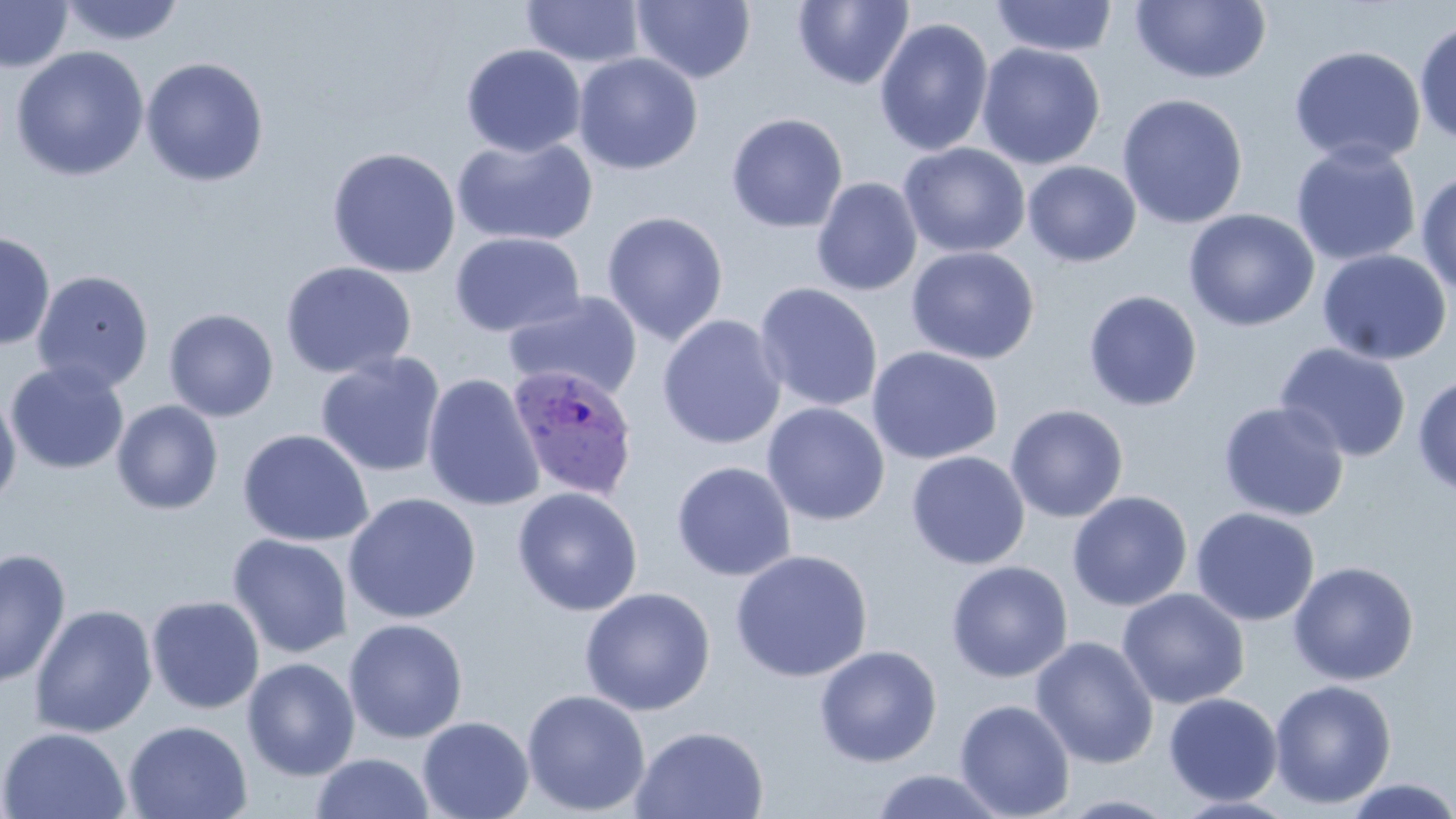 Approximate bounding boxes as [x1, y1, x2, y2] in pixels. Plasmodium ovale-infected red blood cell locations: [506, 364, 639, 501]. Uninfected red blood cell locations: [793, 0, 915, 91], [989, 0, 1119, 58], [0, 1, 73, 72], [58, 1, 187, 47], [519, 1, 646, 68], [631, 1, 757, 84], [1130, 2, 1271, 84], [874, 17, 994, 157], [1413, 19, 1456, 147], [976, 42, 1106, 170], [460, 43, 586, 158], [1288, 44, 1426, 169], [11, 46, 149, 181], [573, 52, 703, 175], [140, 57, 269, 186], [1116, 93, 1249, 229], [726, 113, 848, 233], [452, 135, 598, 248], [1290, 141, 1422, 267], [898, 142, 1031, 259], [326, 147, 461, 279], [1023, 161, 1141, 267], [1415, 170, 1456, 297], [811, 177, 923, 296], [1183, 208, 1320, 332], [601, 210, 729, 345], [0, 230, 56, 351], [449, 231, 586, 338], [905, 246, 1040, 365], [1317, 249, 1452, 365], [280, 260, 417, 380], [31, 270, 154, 394], [754, 282, 883, 413], [1082, 290, 1203, 411], [504, 291, 643, 401], [164, 308, 279, 422], [657, 314, 787, 450], [1274, 343, 1412, 463], [866, 345, 1003, 465], [315, 351, 447, 478], [5, 361, 130, 474], [422, 373, 545, 512], [1413, 374, 1456, 497], [0, 387, 22, 509], [112, 400, 223, 515], [1218, 401, 1350, 522], [761, 403, 890, 526], [1005, 404, 1128, 523], [237, 428, 374, 547], [906, 451, 1030, 570], [671, 461, 797, 582], [511, 486, 643, 616], [1066, 490, 1193, 611], [344, 492, 481, 624], [1190, 507, 1320, 627], [227, 533, 352, 659], [0, 548, 72, 689], [730, 550, 873, 682], [946, 560, 1073, 683], [1288, 561, 1419, 685], [579, 587, 716, 716], [1117, 588, 1249, 709], [146, 595, 265, 715], [29, 604, 157, 738], [343, 618, 468, 743], [1030, 635, 1159, 770], [814, 645, 942, 768], [242, 657, 360, 781], [1269, 679, 1397, 809], [521, 689, 650, 816], [1163, 692, 1283, 806], [954, 698, 1075, 819], [417, 715, 534, 819], [123, 720, 253, 819], [630, 726, 770, 818], [0, 727, 131, 818], [309, 752, 435, 819], [868, 768, 1010, 819], [1342, 777, 1456, 819], [1056, 793, 1183, 818]. Slide-level diagnosis: Plasmodium ovale. Image is 1456×819 pixels. May-Grünwald-Giemsa-stained preparation. Optical microscopy. Single field of view. Thin blood film. 1000x magnification.